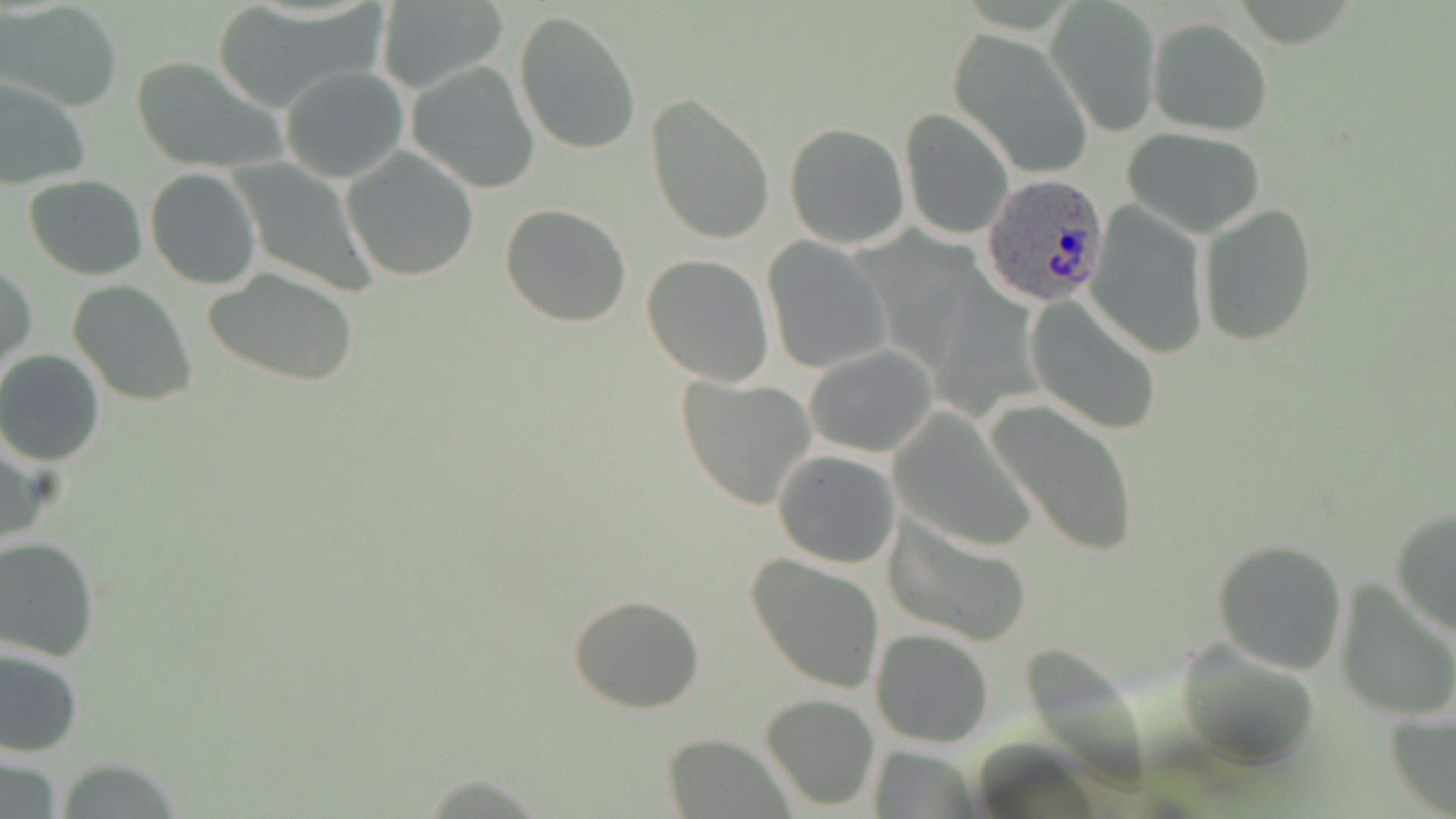

Plasmodium ovale-infected red blood cell locations = approximate bounding boxes as (x1, y1, x2, y2) in pixels: (982, 174, 1110, 308)
slide-level diagnosis = Plasmodium ovale
uninfected red blood cell locations = approximate bounding boxes as (x1, y1, x2, y2) in pixels: (1, 2, 125, 112), (209, 2, 382, 114), (1047, 2, 1160, 133), (373, 4, 512, 97), (512, 9, 643, 155), (1148, 18, 1272, 134), (947, 28, 1094, 178), (129, 56, 282, 171), (406, 61, 540, 194), (280, 65, 408, 184), (0, 77, 90, 190), (646, 94, 775, 245), (899, 107, 1014, 240), (783, 122, 910, 249), (1121, 127, 1266, 238), (342, 148, 479, 282), (230, 160, 379, 296), (144, 168, 260, 289), (22, 175, 147, 280), (1084, 201, 1209, 360), (500, 203, 632, 326), (1197, 204, 1318, 346), (761, 239, 890, 376), (641, 254, 775, 387), (1, 262, 36, 381), (204, 268, 360, 385), (67, 280, 197, 405), (1026, 295, 1163, 435), (804, 343, 940, 458), (0, 351, 105, 465), (678, 375, 815, 509), (986, 397, 1143, 557), (891, 407, 1039, 554), (772, 449, 902, 568), (1389, 505, 1455, 640), (883, 510, 1033, 648), (0, 536, 100, 661), (1211, 538, 1349, 674), (746, 555, 886, 694), (1334, 579, 1456, 721), (569, 596, 704, 714), (871, 629, 995, 748), (1175, 637, 1322, 767), (0, 646, 85, 759), (761, 693, 881, 811), (1384, 705, 1456, 815), (662, 732, 792, 818), (864, 747, 982, 818), (0, 751, 64, 819)
magnification = 1000x
field of view = one of a larger specimen
stain = May-Grünwald-Giemsa
image size = 1456×819 pixels
modality = optical microscopy
preparation = thin blood smear